Locate every uninfected red blood cell.
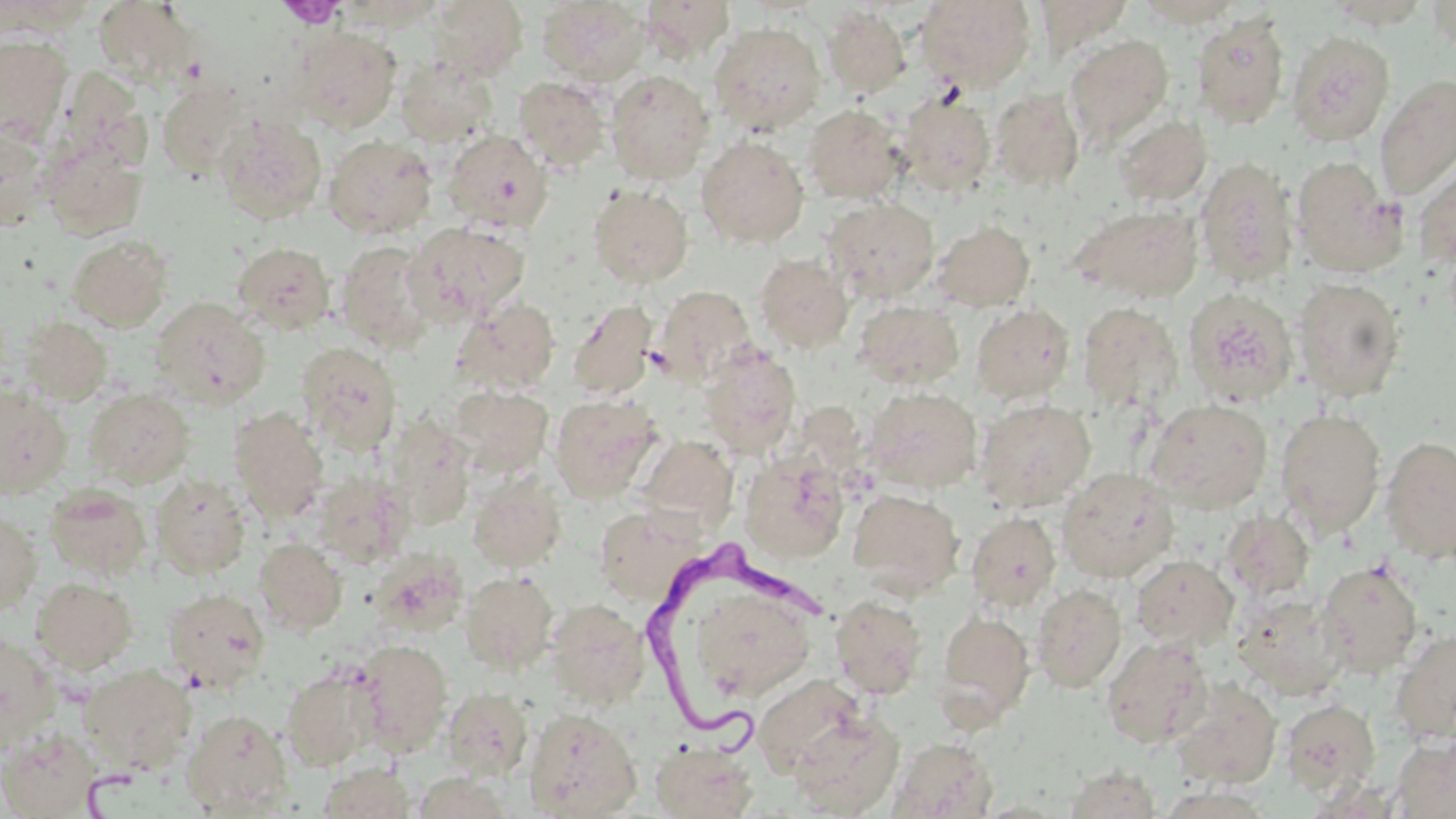
Approximate bounding boxes as (x1,y1)-(x2,y2) corner pairs in pixels.
Uninfected red blood cells: (428,0)-(528,82), (639,0)-(735,62), (916,0)-(1036,92), (1034,0)-(1134,57), (93,1)-(200,87), (537,1)-(651,85), (1134,1)-(1245,28), (1325,1)-(1434,29), (1427,1)-(1456,50), (337,2)-(448,30), (822,6)-(911,99), (1192,12)-(1291,128), (709,21)-(826,135), (292,26)-(401,132), (1287,30)-(1395,145), (0,34)-(73,143), (1064,35)-(1173,146), (396,56)-(497,147), (606,69)-(714,183), (1375,75)-(1456,199), (513,76)-(610,172), (156,78)-(251,178), (989,88)-(1085,192), (898,91)-(996,195), (803,104)-(905,203), (215,114)-(327,224), (1113,114)-(1212,206), (0,128)-(52,231), (443,130)-(553,231), (323,134)-(437,238), (697,136)-(809,249), (41,141)-(147,239), (1414,153)-(1456,269), (1291,155)-(1405,277), (1195,157)-(1299,285), (589,185)-(693,287), (824,197)-(940,301), (1069,205)-(1204,302), (932,219)-(1035,311), (407,221)-(530,324), (67,235)-(173,331), (334,240)-(437,352), (233,241)-(336,333), (754,253)-(854,353), (1293,278)-(1407,400), (653,285)-(756,387), (1183,288)-(1299,407), (151,297)-(270,408), (452,298)-(560,395), (567,299)-(660,401), (854,300)-(965,390), (1078,301)-(1183,411), (972,303)-(1076,403), (20,317)-(112,404), (297,341)-(402,452), (698,345)-(801,456), (448,385)-(553,476), (0,386)-(72,497), (863,387)-(982,492), (83,388)-(195,487), (550,393)-(663,504), (974,398)-(1096,511), (1147,398)-(1273,513), (1275,408)-(1385,536), (229,409)-(329,521), (385,417)-(476,528), (638,435)-(739,530), (1381,436)-(1456,564), (741,452)-(850,562), (1057,467)-(1178,582), (315,472)-(413,568), (151,473)-(252,578), (468,473)-(566,571), (157,475)-(256,691), (44,483)-(152,580), (847,489)-(965,596), (595,505)-(704,605), (1221,509)-(1314,601), (0,510)-(42,614), (966,511)-(1060,612), (255,537)-(348,635), (370,549)-(469,637), (1130,555)-(1238,650), (1317,560)-(1423,677), (460,571)-(558,673), (31,577)-(138,674), (683,580)-(817,706), (1032,583)-(1127,693), (163,587)-(270,692), (1233,592)-(1350,700), (830,595)-(928,699), (546,598)-(651,709), (936,608)-(1035,726), (1389,629)-(1456,745), (0,632)-(59,750), (1102,636)-(1214,748), (354,638)-(453,755), (79,664)-(196,774), (281,667)-(380,770), (752,674)-(866,777), (1170,677)-(1282,789), (442,687)-(533,778), (1280,699)-(1380,797), (525,707)-(642,818), (182,708)-(293,815), (788,710)-(904,817), (0,727)-(100,818), (1391,736)-(1455,818), (889,737)-(998,818), (651,741)-(759,818), (319,762)-(415,818), (1064,764)-(1161,818), (410,770)-(516,818).

slide-level diagnosis = Trypanosoma brucei
modality = light microscopy
stain = May-Grünwald-Giemsa
platelet locations = approximate bounding boxes as (x1,y1)-(x2,y2) corner pairs in pixels: (278,0)-(346,29)
image size = 1456×819 pixels
magnification = 1000x
preparation = thin blood film
field of view = one of a larger specimen
Trypanosoma brucei locations = approximate bounding boxes as (x1,y1)-(x2,y2) corner pairs in pixels: (637,538)-(835,763)